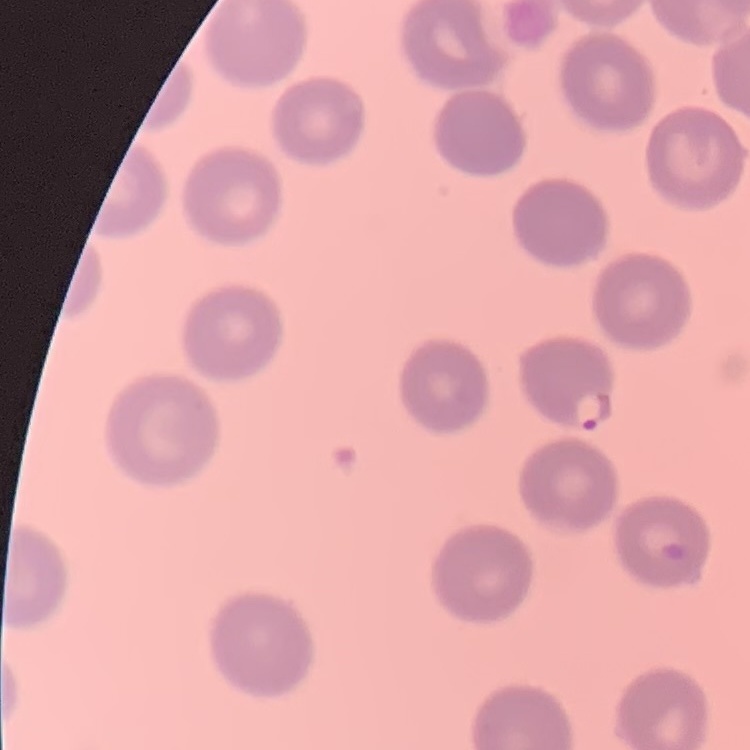
Summary:
  - Erythrocyte morphology: no rouleaux formation
  - Image type: one tile cut from a larger photomicrograph
  - Stain: Field's or Giemsa
  - Preparation: thin blood smear